Report the malaria status of this cell.
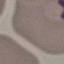
Parasitized.

Summary:
  - Capture: smartphone camera at the microscope eyepiece
  - Image type: automatically extracted cell patch, resized to 64 × 64 pixels
  - Preparation: thin blood smear
  - Stain: Giemsa